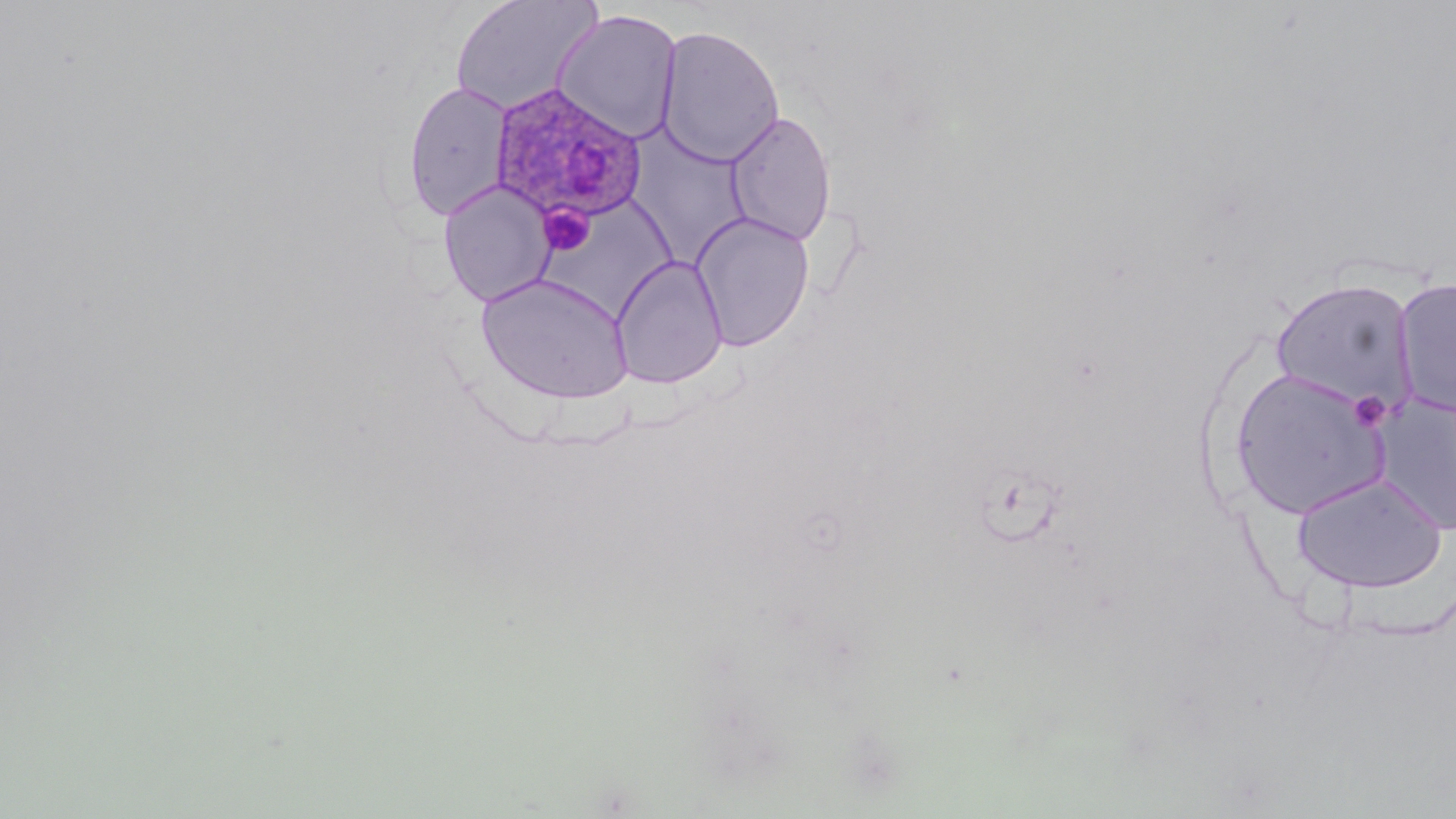 Approximate bounding boxes as [x1, y1, x2, y2] in pixels. Plasmodium ovale-infected red blood cell locations: [489, 83, 649, 226]. Uninfected red blood cell locations: [449, 0, 603, 116], [551, 9, 683, 143], [656, 25, 785, 168], [402, 80, 515, 222], [724, 109, 838, 248], [627, 117, 757, 274], [438, 180, 555, 306], [535, 199, 689, 321], [690, 211, 815, 352], [611, 255, 727, 389], [475, 273, 636, 404], [1392, 277, 1456, 419], [1269, 278, 1419, 413], [1230, 367, 1393, 519], [1372, 393, 1456, 535], [1291, 472, 1449, 593]. Platelet locations: [536, 203, 596, 257], [1348, 390, 1391, 433]. Slide-level diagnosis: Plasmodium ovale. Light microscopy. May-Grünwald-Giemsa-stained preparation. Thin blood film. Single field of view. Image is 1456×819 pixels. 1000x magnification.